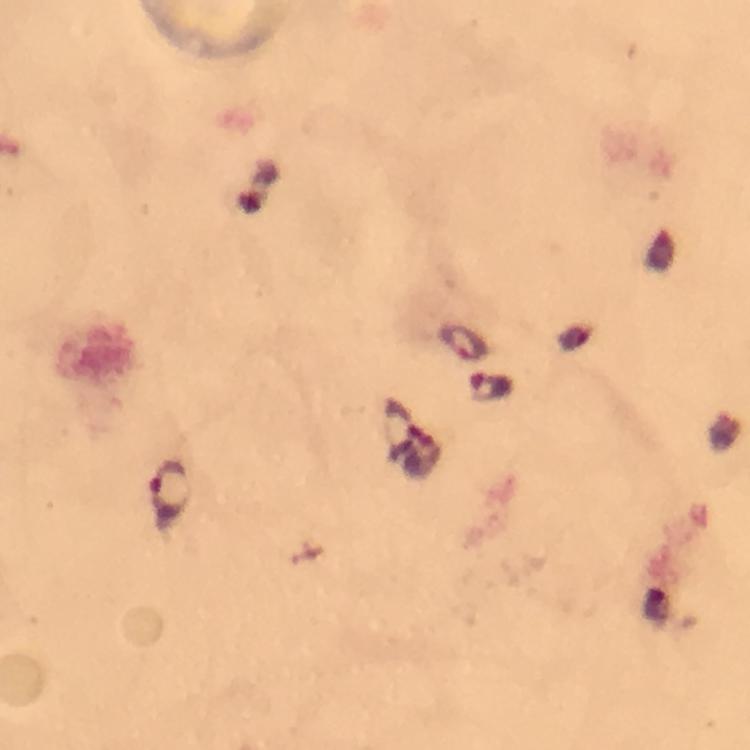

Approximate centers as (x, y) in pixels.
Summary:
  - Plasmodium parasite locations: (462, 341), (492, 388), (403, 419), (169, 490)
  - Context: from a malaria diagnostic workup
  - Immersion oil: used
  - Image size: 750×750 pixels
  - Magnification: 100x
  - Preparation: thick smear
  - Stain: Giemsa
  - Capture: smartphone mounted on the microscope
  - Cropped from: a single field of view